Name the blood parasite species.
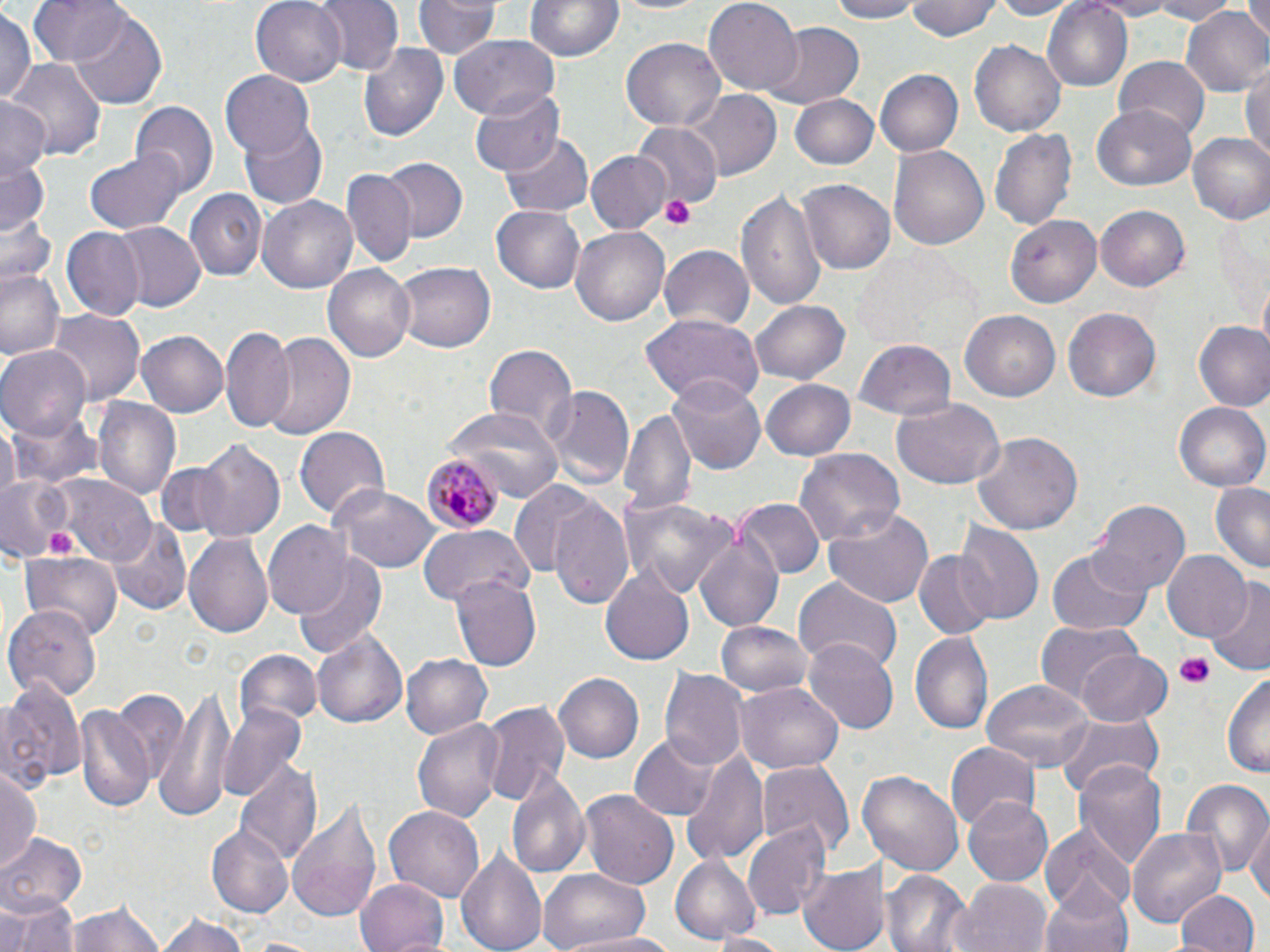

Plasmodium malariae.

preparation = thin blood film
magnification = 1000x
uninfected red blood cell locations = approximate bounding boxes as (x1, y1, x2, y2) in pixels: (30, 0, 132, 67), (253, 0, 347, 87), (315, 0, 402, 77), (520, 0, 625, 63), (603, 0, 716, 17), (705, 0, 802, 91), (827, 0, 920, 23), (906, 0, 1000, 42), (987, 0, 1078, 20), (1043, 0, 1132, 90), (1076, 0, 1181, 18), (1139, 0, 1239, 23), (1244, 0, 1270, 42), (416, 1, 501, 60), (0, 7, 36, 108), (1181, 7, 1269, 97), (68, 12, 168, 110), (761, 23, 865, 108), (447, 34, 560, 118), (621, 37, 726, 130), (970, 38, 1069, 138), (357, 40, 448, 145), (1114, 56, 1210, 139), (7, 58, 104, 164), (1242, 61, 1270, 164), (874, 66, 964, 156), (219, 71, 315, 161), (469, 87, 564, 176), (684, 91, 781, 181), (789, 94, 880, 171), (0, 96, 50, 180), (130, 102, 217, 199), (1091, 106, 1198, 191), (239, 118, 328, 209), (632, 123, 720, 208), (990, 126, 1076, 231), (500, 130, 592, 217), (1186, 132, 1270, 225), (890, 144, 989, 252), (84, 150, 190, 235), (584, 150, 671, 234), (378, 158, 468, 244), (0, 159, 50, 238), (342, 170, 415, 268), (799, 178, 896, 275), (186, 189, 266, 280), (735, 190, 825, 311), (258, 196, 357, 294), (490, 203, 587, 292), (1095, 204, 1189, 292), (999, 212, 1122, 305), (4, 215, 57, 288), (114, 222, 205, 309), (570, 225, 672, 326), (60, 227, 143, 322), (659, 242, 754, 329), (854, 248, 970, 348), (390, 262, 496, 354), (1, 265, 65, 362), (325, 265, 416, 363), (751, 299, 849, 385), (1064, 306, 1164, 403), (49, 310, 143, 408), (640, 312, 765, 406), (961, 312, 1060, 402), (1193, 321, 1270, 411), (136, 329, 227, 416), (220, 329, 296, 429), (261, 329, 356, 440), (854, 339, 958, 422), (485, 343, 577, 442), (0, 346, 90, 441), (668, 374, 766, 475), (762, 379, 858, 460), (544, 384, 633, 487), (890, 396, 1006, 491), (92, 397, 181, 503), (1175, 403, 1268, 490), (618, 404, 697, 516), (445, 406, 564, 499), (7, 410, 103, 490), (295, 425, 389, 522), (972, 429, 1083, 537), (194, 441, 285, 541), (792, 449, 903, 547), (152, 461, 235, 541), (55, 476, 154, 562), (0, 478, 74, 559), (510, 482, 612, 588), (1208, 483, 1270, 575), (330, 486, 437, 574), (551, 496, 638, 612), (622, 496, 733, 600), (734, 498, 824, 579), (1088, 500, 1191, 597), (824, 508, 935, 608), (109, 519, 192, 618), (956, 520, 1042, 626), (263, 521, 353, 620), (418, 525, 532, 608), (184, 529, 274, 640), (694, 529, 785, 635), (1046, 549, 1154, 636), (1163, 550, 1254, 642), (21, 551, 123, 642), (914, 551, 998, 640), (296, 555, 387, 656), (599, 567, 695, 668), (450, 577, 540, 670), (793, 577, 902, 674), (1207, 584, 1270, 674), (8, 604, 102, 705), (716, 619, 814, 699), (1034, 620, 1141, 708), (311, 626, 407, 732), (911, 632, 993, 735), (803, 636, 898, 732), (232, 648, 323, 731), (1073, 648, 1174, 728), (400, 652, 493, 738), (660, 669, 748, 773), (1223, 669, 1270, 781), (556, 673, 644, 763), (155, 676, 235, 823), (0, 678, 86, 795), (981, 679, 1095, 776), (735, 681, 842, 776), (109, 688, 193, 791), (218, 700, 308, 804), (479, 700, 571, 807), (76, 701, 156, 816), (1055, 712, 1163, 800), (415, 716, 507, 824), (631, 734, 718, 819), (946, 743, 1037, 834), (681, 749, 769, 867), (1073, 758, 1166, 870), (756, 762, 853, 855), (0, 764, 42, 874), (235, 765, 321, 868), (507, 768, 590, 879), (858, 769, 964, 877), (1181, 778, 1269, 882), (581, 792, 677, 887), (962, 794, 1053, 884), (288, 796, 382, 925), (386, 805, 484, 902), (1246, 818, 1270, 912), (742, 821, 832, 919), (1042, 824, 1132, 915), (1128, 824, 1229, 928), (207, 825, 291, 917), (0, 832, 87, 917), (455, 845, 547, 952), (669, 853, 760, 944), (797, 862, 888, 952), (537, 868, 652, 952), (882, 872, 973, 952), (356, 876, 452, 952), (956, 877, 1054, 952), (1038, 878, 1136, 952), (1176, 890, 1258, 952), (3, 895, 79, 952), (67, 897, 168, 952), (153, 910, 253, 951), (709, 932, 796, 951), (575, 933, 680, 952)
Plasmodium malariae-infected red blood cell locations = approximate bounding boxes as (x1, y1, x2, y2) in pixels: (420, 452, 499, 533)
platelet locations = approximate bounding boxes as (x1, y1, x2, y2) in pixels: (658, 193, 697, 231), (1176, 651, 1217, 690)
stain = May-Grünwald-Giemsa
field of view = one of a larger specimen
image size = 1270×952 pixels
modality = light microscopy